Comment on the morphology of the erythrocytes.
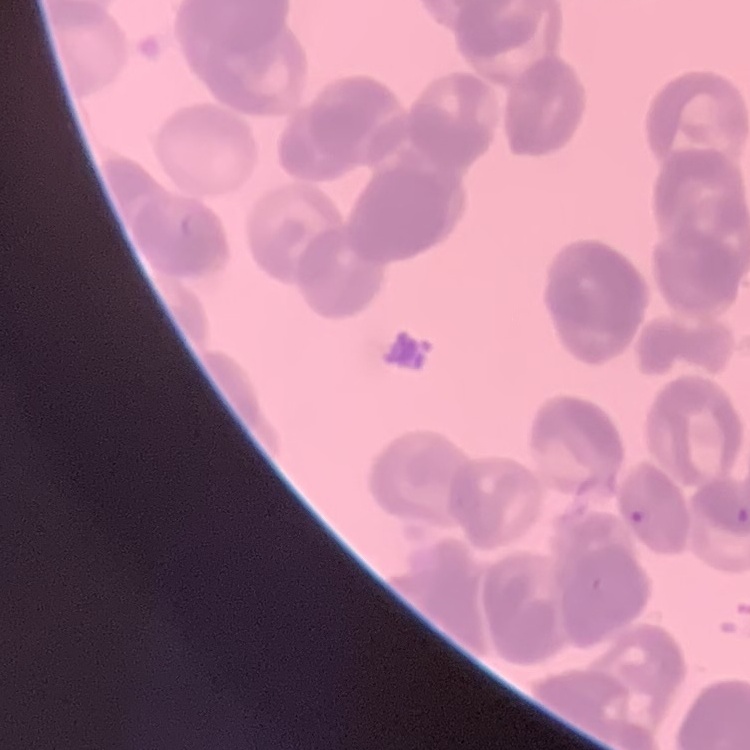
They show rouleaux formation.

Field's or Giemsa stain. Thin blood film. Square crop of a larger photomicrograph.